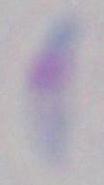

Summary:
  - Identification: Toxoplasma gondii
  - Modality: photomicrograph
  - Magnification: 1000x